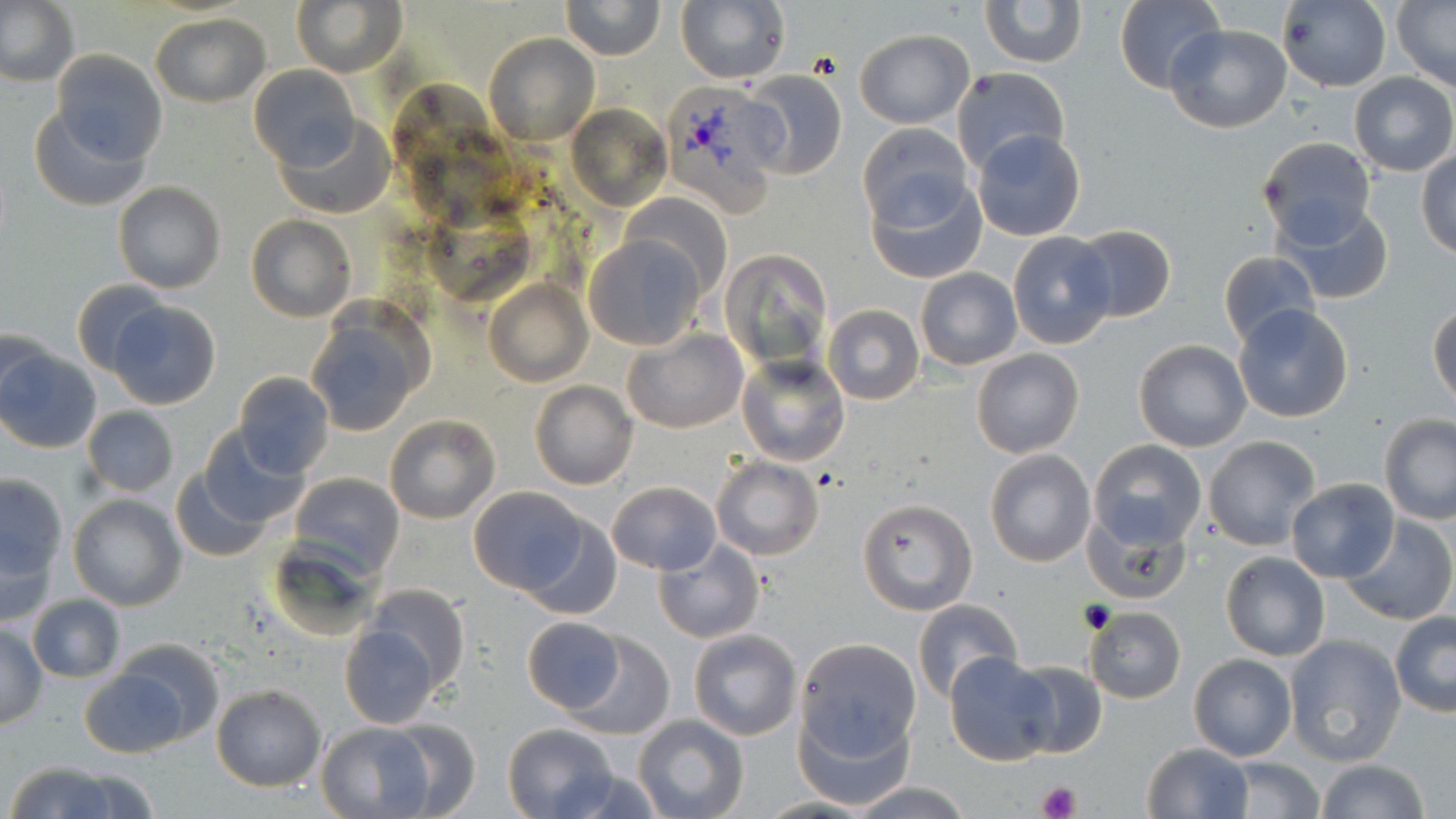
Summary:
  - Coordinate format: approximate bounding boxes as named x1/y1/x2/y2 corners in pixels
  - Uninfected red blood cell locations: (x1=0, y1=0, x2=79, y2=88), (x1=293, y1=0, x2=406, y2=76), (x1=559, y1=0, x2=666, y2=61), (x1=979, y1=0, x2=1086, y2=70), (x1=1113, y1=0, x2=1225, y2=93), (x1=1277, y1=0, x2=1391, y2=91), (x1=676, y1=1, x2=790, y2=86), (x1=1392, y1=1, x2=1456, y2=90), (x1=150, y1=13, x2=270, y2=106), (x1=1164, y1=23, x2=1292, y2=132), (x1=855, y1=29, x2=974, y2=127), (x1=484, y1=34, x2=599, y2=145), (x1=50, y1=51, x2=168, y2=167), (x1=251, y1=65, x2=359, y2=169), (x1=952, y1=67, x2=1072, y2=176), (x1=737, y1=68, x2=849, y2=181), (x1=1350, y1=72, x2=1456, y2=176), (x1=28, y1=101, x2=151, y2=211), (x1=567, y1=102, x2=672, y2=212), (x1=275, y1=112, x2=395, y2=221), (x1=857, y1=124, x2=973, y2=234), (x1=972, y1=129, x2=1085, y2=240), (x1=1258, y1=136, x2=1376, y2=244), (x1=1418, y1=149, x2=1456, y2=259), (x1=868, y1=166, x2=987, y2=283), (x1=112, y1=181, x2=226, y2=294), (x1=624, y1=193, x2=731, y2=299), (x1=1276, y1=198, x2=1393, y2=306), (x1=246, y1=215, x2=356, y2=322), (x1=1069, y1=224, x2=1177, y2=322), (x1=1007, y1=231, x2=1119, y2=349), (x1=584, y1=234, x2=706, y2=350), (x1=721, y1=249, x2=833, y2=375), (x1=1218, y1=250, x2=1321, y2=350), (x1=915, y1=267, x2=1022, y2=370), (x1=484, y1=277, x2=593, y2=387), (x1=73, y1=278, x2=172, y2=376), (x1=107, y1=301, x2=220, y2=410), (x1=1429, y1=303, x2=1456, y2=409), (x1=823, y1=304, x2=923, y2=405), (x1=1233, y1=304, x2=1356, y2=422), (x1=304, y1=309, x2=429, y2=438), (x1=0, y1=325, x2=58, y2=420), (x1=622, y1=328, x2=748, y2=434), (x1=1134, y1=339, x2=1252, y2=452), (x1=972, y1=348, x2=1083, y2=458), (x1=0, y1=349, x2=102, y2=454), (x1=736, y1=353, x2=851, y2=468), (x1=233, y1=372, x2=334, y2=477), (x1=531, y1=381, x2=638, y2=490), (x1=83, y1=407, x2=178, y2=496), (x1=384, y1=413, x2=501, y2=524), (x1=1378, y1=414, x2=1456, y2=525), (x1=200, y1=429, x2=309, y2=527), (x1=1204, y1=436, x2=1320, y2=549), (x1=1087, y1=439, x2=1207, y2=549), (x1=985, y1=449, x2=1096, y2=567), (x1=712, y1=457, x2=823, y2=561), (x1=169, y1=469, x2=273, y2=564), (x1=0, y1=472, x2=68, y2=579), (x1=289, y1=472, x2=405, y2=577), (x1=1284, y1=478, x2=1400, y2=584), (x1=607, y1=481, x2=721, y2=575), (x1=468, y1=486, x2=586, y2=595), (x1=67, y1=493, x2=188, y2=611), (x1=857, y1=498, x2=977, y2=614), (x1=1083, y1=509, x2=1193, y2=608), (x1=524, y1=514, x2=623, y2=620), (x1=1338, y1=515, x2=1456, y2=625), (x1=1, y1=530, x2=60, y2=628), (x1=654, y1=539, x2=765, y2=643), (x1=1221, y1=551, x2=1329, y2=661), (x1=362, y1=583, x2=469, y2=693), (x1=26, y1=593, x2=125, y2=683), (x1=913, y1=600, x2=1025, y2=704), (x1=1084, y1=606, x2=1186, y2=704), (x1=1390, y1=612, x2=1455, y2=716), (x1=521, y1=618, x2=625, y2=713), (x1=338, y1=624, x2=439, y2=728), (x1=0, y1=625, x2=47, y2=728), (x1=689, y1=629, x2=802, y2=741), (x1=568, y1=632, x2=674, y2=741), (x1=1284, y1=634, x2=1406, y2=765), (x1=110, y1=638, x2=226, y2=746), (x1=795, y1=638, x2=921, y2=759), (x1=1188, y1=652, x2=1297, y2=762), (x1=945, y1=653, x2=1059, y2=765), (x1=1007, y1=659, x2=1107, y2=760), (x1=79, y1=667, x2=188, y2=759), (x1=211, y1=684, x2=326, y2=791), (x1=799, y1=703, x2=912, y2=809), (x1=632, y1=714, x2=749, y2=819), (x1=380, y1=721, x2=480, y2=818), (x1=315, y1=722, x2=439, y2=818), (x1=502, y1=722, x2=619, y2=819), (x1=1141, y1=742, x2=1252, y2=819), (x1=1216, y1=756, x2=1328, y2=819), (x1=1312, y1=759, x2=1433, y2=818), (x1=3, y1=763, x2=131, y2=819), (x1=552, y1=765, x2=667, y2=818), (x1=54, y1=769, x2=161, y2=819), (x1=848, y1=781, x2=976, y2=818)
  - Platelet locations: (x1=1037, y1=781, x2=1079, y2=819)
  - Plasmodium vivax-infected red blood cell locations: (x1=665, y1=83, x2=797, y2=227)
  - Slide-level diagnosis: Plasmodium vivax
  - Modality: optical microscopy
  - Magnification: 1000x
  - Stain: May-Grünwald-Giemsa
  - Image size: 1456×819 pixels
  - Preparation: thin blood smear
  - Field of view: single